Report the malaria status of this cell.
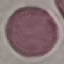
It is uninfected.

stain = Giemsa
capture = smartphone camera at the microscope eyepiece
preparation = thin blood film
image type = automatically extracted cell patch, resized to 64 × 64 pixels